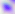
Toxoplasma gondii is seen. Captured at 400x magnification. Micrograph.